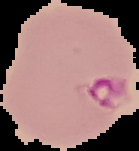
malaria status = parasitized
image type = segmented cell region on a black background
preparation = thin blood smear
image size = 139×151 pixels